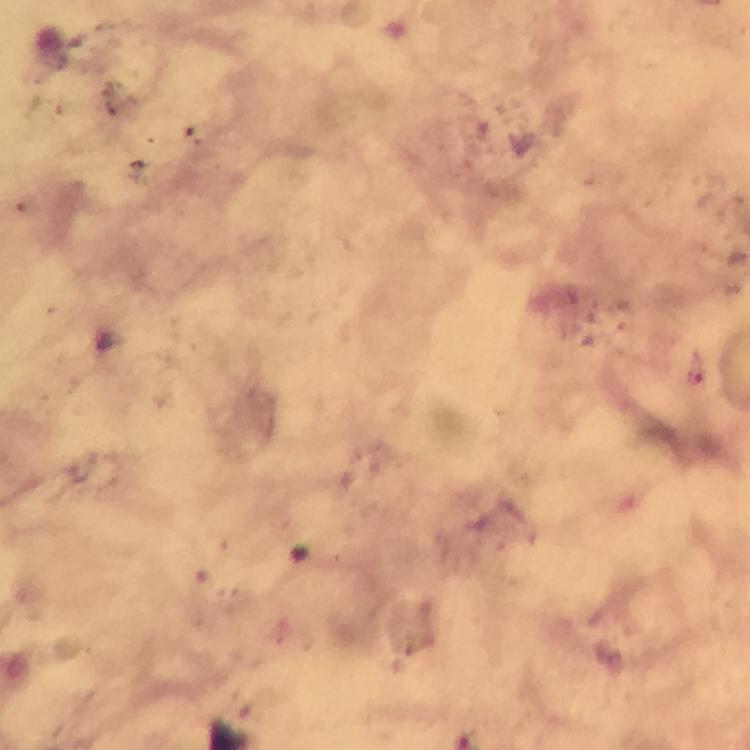
Approximate object centers, in pixels from the top-left corner.
Summary:
  - Plasmodium parasite locations: (x=694, y=369)
  - Magnification: 100x
  - Context: from a diagnostic examination for malaria
  - Cropped from: one field of view
  - Immersion oil: applied
  - Stain: Giemsa
  - Image size: 750×750 pixels
  - Preparation: thick blood smear
  - Capture: smartphone camera through the microscope